State the preparation type.
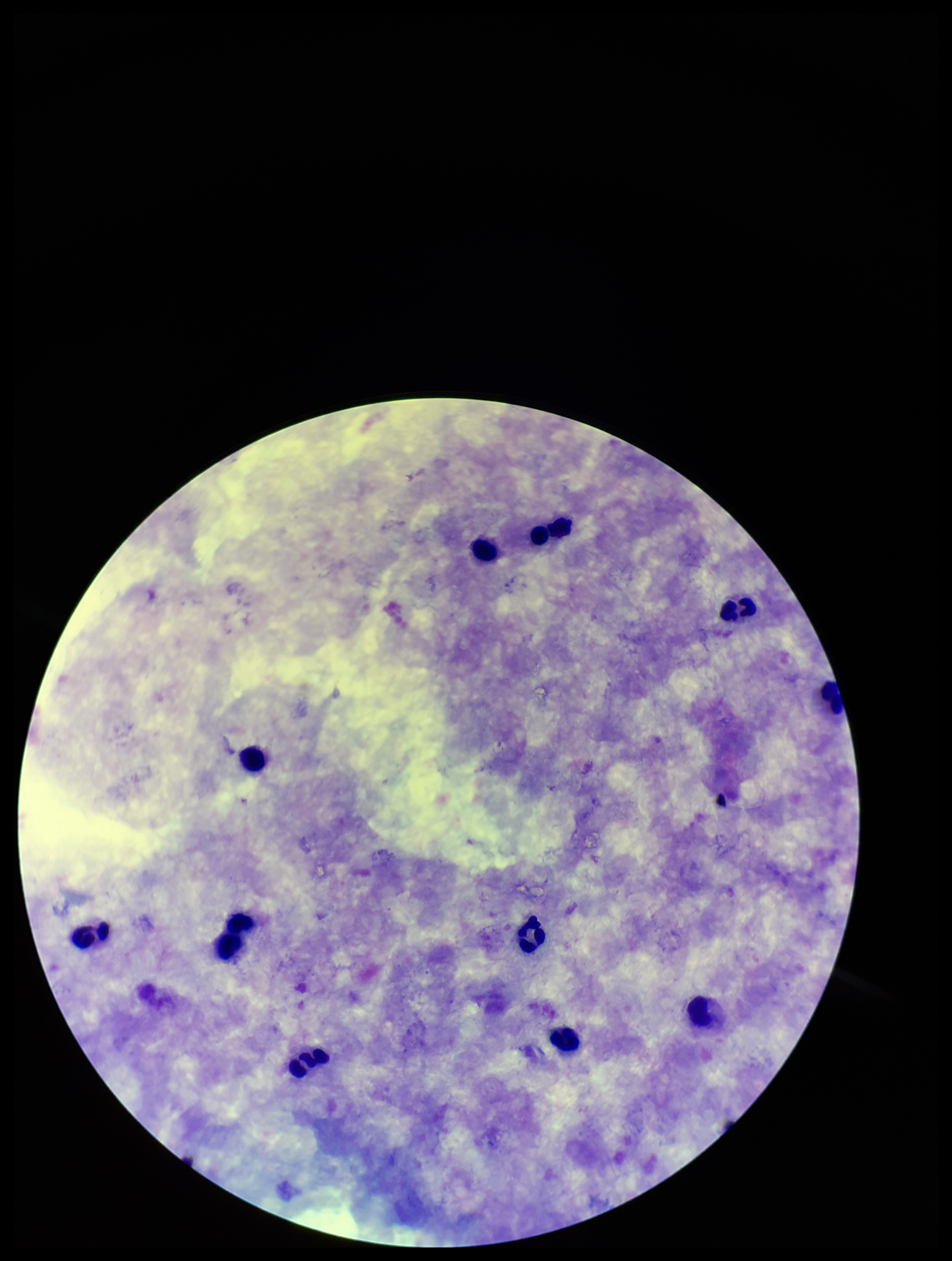

Thick.

Summary:
  - Patient malaria status: negative
  - Capture: smartphone photograph through the microscope eyepiece
  - Image size: 952×1261 pixels
  - Parasite count: 0
  - Plasmodium parasites: none identified
  - Leukocyte count: 11
  - Field of view: one from this slide
  - Stain: Giemsa